Assess the morphology of the erythrocytes.
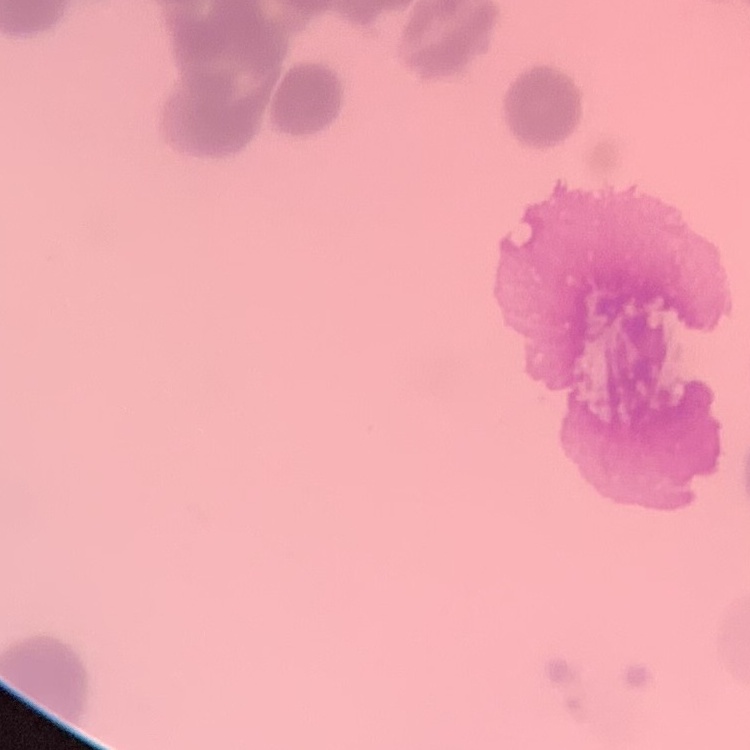

They show rouleaux formation.

Square crop of a larger photomicrograph. Stained with either Field's or Giemsa. Thin blood smear.